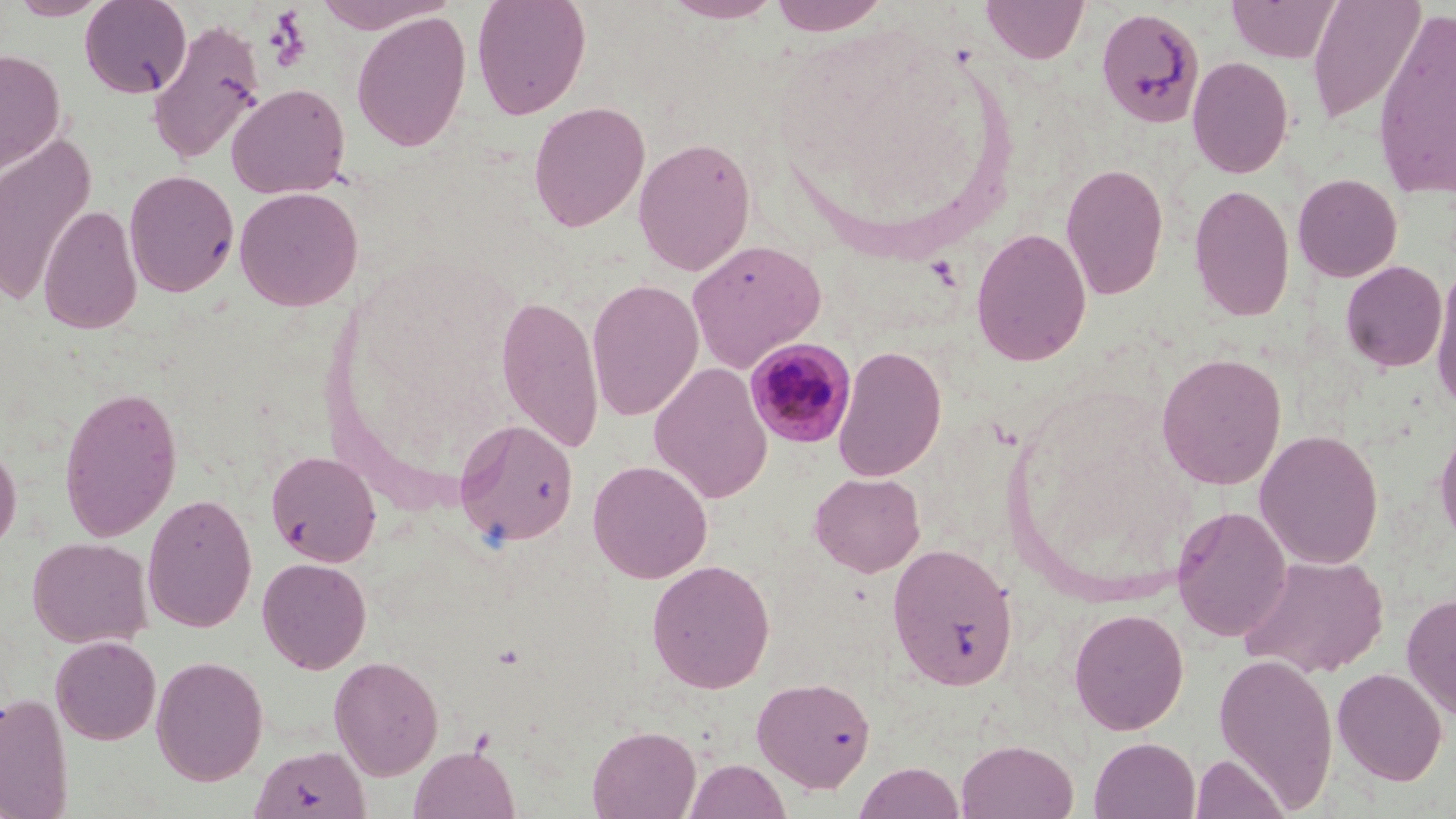
Summary:
  - Coordinate format: approximate bounding boxes as [x1, y1, x2, y2] in pixels
  - Plasmodium malariae-infected red blood cell locations: [744, 338, 857, 448]
  - Uninfected red blood cell locations: [7, 0, 111, 20], [79, 0, 192, 98], [312, 0, 457, 33], [471, 0, 592, 120], [662, 0, 783, 23], [768, 0, 892, 35], [981, 0, 1089, 64], [1228, 0, 1340, 63], [1306, 0, 1425, 125], [1095, 7, 1205, 128], [351, 11, 472, 153], [1371, 11, 1455, 199], [147, 18, 267, 166], [0, 48, 66, 175], [1187, 55, 1294, 179], [226, 83, 350, 199], [528, 101, 650, 232], [0, 133, 97, 308], [633, 136, 757, 276], [1060, 162, 1169, 300], [123, 170, 239, 297], [1292, 173, 1402, 282], [1189, 182, 1295, 323], [233, 186, 363, 311], [39, 205, 142, 334], [971, 227, 1092, 366], [687, 238, 827, 372], [1340, 260, 1448, 373], [1429, 265, 1456, 409], [586, 278, 704, 422], [496, 295, 604, 454], [832, 344, 947, 482], [1155, 352, 1288, 490], [648, 362, 773, 503], [59, 386, 182, 542], [454, 418, 579, 548], [1434, 418, 1456, 553], [1254, 429, 1384, 570], [0, 437, 22, 558], [265, 450, 381, 567], [587, 459, 713, 583], [810, 472, 925, 577], [142, 493, 257, 633], [1171, 505, 1292, 643], [27, 537, 153, 649], [886, 542, 1018, 690], [1239, 554, 1389, 679], [257, 557, 372, 675], [646, 559, 776, 693], [1401, 592, 1456, 721], [1068, 607, 1188, 735], [51, 636, 161, 745], [1213, 652, 1339, 812], [151, 655, 269, 785], [329, 655, 444, 780], [1332, 667, 1448, 786], [752, 676, 876, 793], [0, 690, 74, 818], [587, 724, 701, 819], [1089, 736, 1201, 819], [956, 738, 1079, 819], [251, 744, 370, 818], [409, 744, 520, 819], [1189, 753, 1290, 819], [685, 758, 791, 819], [854, 761, 965, 819]
  - Slide-level diagnosis: Plasmodium malariae
  - Modality: light microscopy
  - Image size: 1456×819 pixels
  - Field of view: one of a larger specimen
  - Magnification: 1000x
  - Stain: May-Grünwald-Giemsa
  - Preparation: thin blood smear